Report the malaria status of this cell.
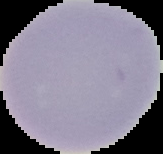
It is uninfected.

Image is 163×154 pixels. From a thin blood smear. Segmented cell region on a black background.